Name the parasite shown.
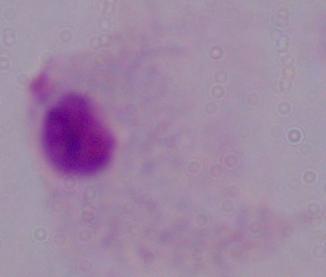
This is a trichomonad.

Captured at 1000x magnification. Photomicrograph.